Outline each blood parasite and name the species.
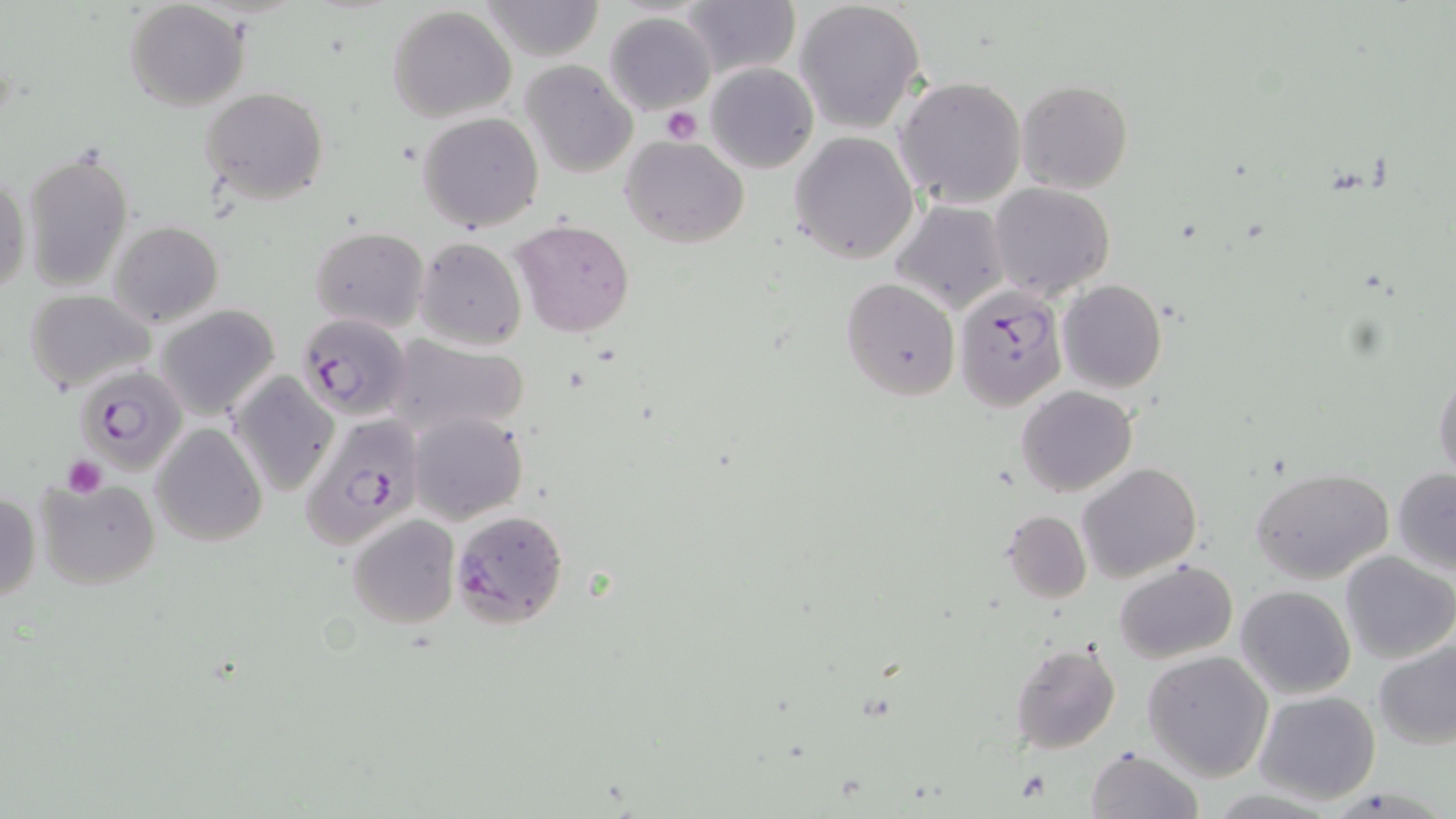
Approximate bounding boxes as (x1,y1)-(x2,y2) corner pairs in pixels.
Plasmodium falciparum-infected red blood cells: (951,286)-(1066,409), (296,313)-(411,421), (75,364)-(186,477), (299,413)-(422,554), (450,508)-(569,627).
No Plasmodium ovale, Plasmodium malariae, Plasmodium vivax, Babesia divergens, or Trypanosoma brucei observed.

slide-level diagnosis = Plasmodium falciparum
stain = May-Grünwald-Giemsa
platelet locations = approximate bounding boxes as (x1,y1)-(x2,y2) corner pairs in pixels: (660,105)-(703,144), (61,456)-(107,497)
modality = light microscopy
image size = 1456×819 pixels
uninfected red blood cell locations = approximate bounding boxes as (x1,y1)-(x2,y2) corner pairs in pixels: (480,0)-(606,62), (124,1)-(250,113), (794,1)-(925,133), (680,2)-(799,80), (387,6)-(517,124), (604,12)-(716,115), (521,61)-(637,179), (705,64)-(816,174), (895,76)-(1026,210), (1015,80)-(1133,195), (200,87)-(329,204), (418,111)-(544,232), (790,132)-(919,263), (621,136)-(750,249), (22,146)-(134,294), (1,169)-(29,301), (989,183)-(1114,301), (892,199)-(1010,315), (513,219)-(635,337), (109,221)-(224,329), (310,227)-(429,333), (416,238)-(525,350), (840,277)-(960,401), (1056,280)-(1167,393), (24,290)-(154,392), (154,304)-(281,420), (392,338)-(528,435), (1432,363)-(1456,482), (227,372)-(338,496), (1016,385)-(1139,497), (409,412)-(527,523), (152,423)-(267,548), (1077,463)-(1202,583), (1252,467)-(1394,585), (1393,468)-(1456,574), (35,477)-(159,589), (1,490)-(42,602), (1003,510)-(1091,603), (349,515)-(460,628), (1338,551)-(1454,665), (1114,561)-(1238,664), (1235,585)-(1356,699), (1373,637)-(1455,750), (1010,641)-(1123,754), (1143,650)-(1273,781), (1254,691)-(1381,805), (1084,747)-(1201,819)
field of view = one of a larger specimen
preparation = thin blood smear
magnification = 1000x